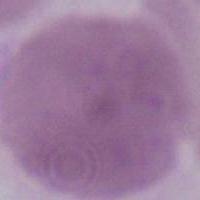
Summary:
  - Modality: micrograph
  - Magnification: 1000x
  - Identification: red blood cell